Classify this cell by malaria status.
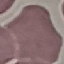

Uninfected.

Thin smear of blood. Acquired by smartphone through the microscope eyepiece. Automatically extracted cell patch, resized to 64 × 64 pixels. Giemsa-stained preparation.